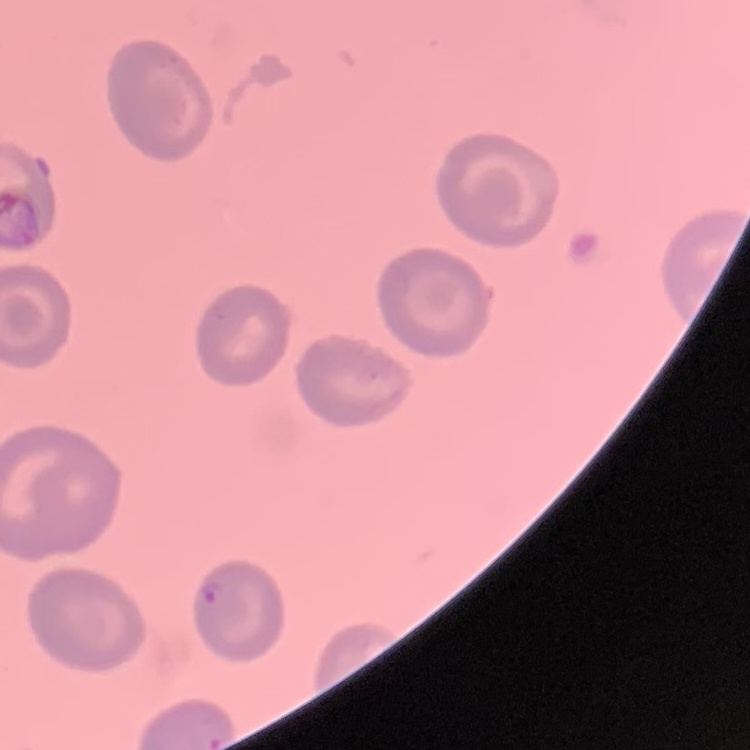
Summary:
  - Red blood cell morphology: no rouleaux formation
  - Stain: Field's or Giemsa
  - Preparation: thin blood smear
  - Image type: one tile cut from a larger photomicrograph